Outline each Plasmodium vivax-infected red blood cell.
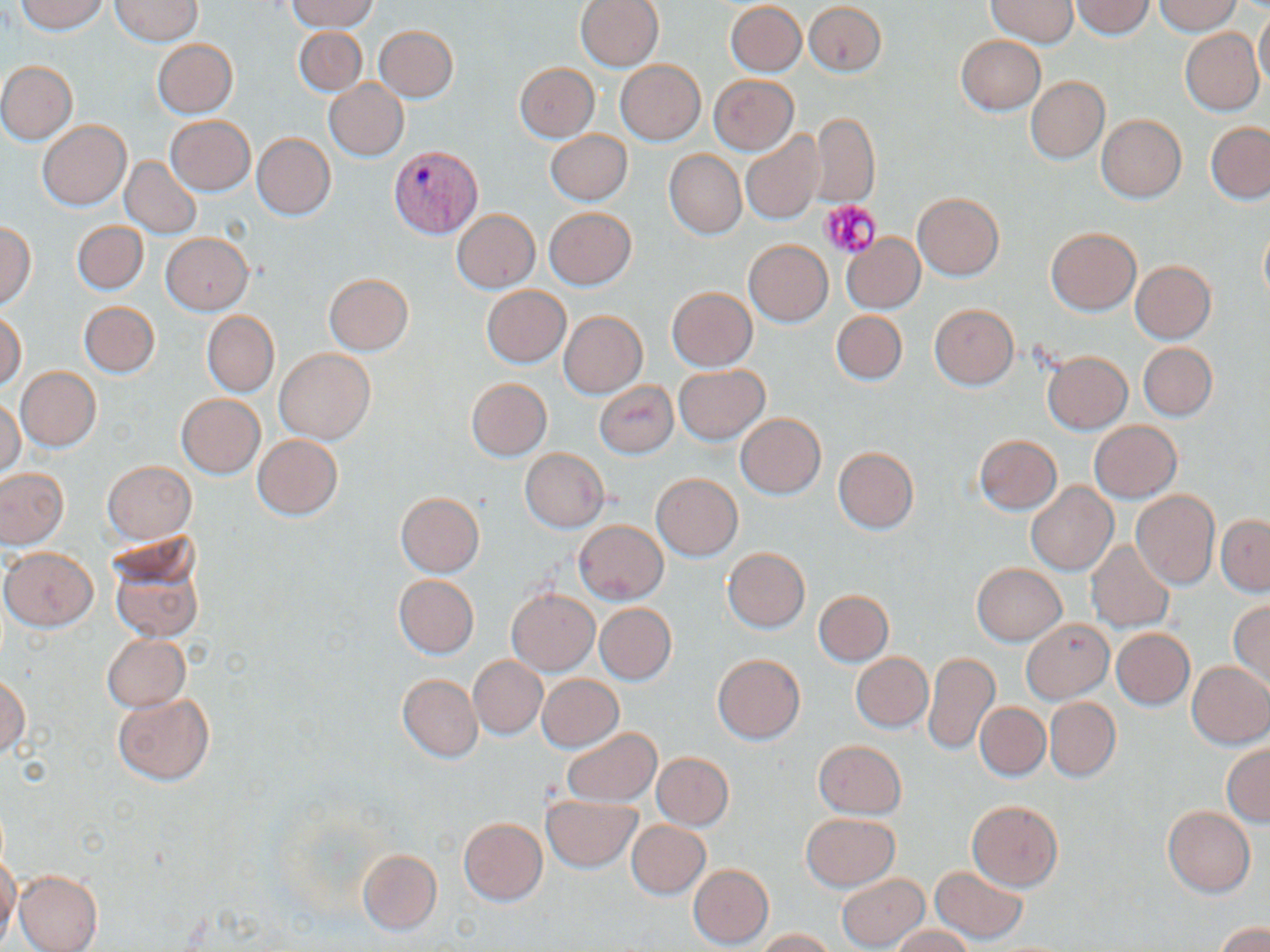
Approximate bounding boxes as named x1/y1/x2/y2 corners in pixels.
Plasmodium vivax-infected red blood cells: (x1=390, y1=151, x2=481, y2=240).

slide-level diagnosis = Plasmodium vivax
magnification = 1000x
platelet locations = approximate bounding boxes as named x1/y1/x2/y2 corners in pixels: (x1=821, y1=200, x2=883, y2=259)
stain = May-Grünwald-Giemsa
preparation = thin blood film
uninfected red blood cell locations = approximate bounding boxes as named x1/y1/x2/y2 corners in pixels: (x1=16, y1=0, x2=107, y2=35), (x1=109, y1=0, x2=202, y2=45), (x1=288, y1=0, x2=375, y2=33), (x1=575, y1=0, x2=664, y2=72), (x1=986, y1=0, x2=1078, y2=48), (x1=1070, y1=0, x2=1154, y2=39), (x1=1151, y1=0, x2=1242, y2=35), (x1=725, y1=2, x2=806, y2=76), (x1=803, y1=2, x2=887, y2=76), (x1=1254, y1=8, x2=1270, y2=90), (x1=374, y1=25, x2=458, y2=102), (x1=293, y1=26, x2=367, y2=96), (x1=1180, y1=28, x2=1264, y2=116), (x1=956, y1=35, x2=1046, y2=115), (x1=152, y1=39, x2=238, y2=119), (x1=615, y1=59, x2=706, y2=145), (x1=1, y1=61, x2=76, y2=144), (x1=514, y1=63, x2=599, y2=142), (x1=709, y1=74, x2=798, y2=155), (x1=1027, y1=77, x2=1109, y2=164), (x1=324, y1=80, x2=408, y2=161), (x1=812, y1=112, x2=879, y2=206), (x1=1097, y1=114, x2=1186, y2=202), (x1=166, y1=117, x2=254, y2=196), (x1=37, y1=120, x2=130, y2=211), (x1=1205, y1=122, x2=1270, y2=204), (x1=545, y1=130, x2=631, y2=205), (x1=740, y1=132, x2=825, y2=225), (x1=252, y1=134, x2=334, y2=220), (x1=664, y1=150, x2=746, y2=239), (x1=121, y1=157, x2=201, y2=238), (x1=912, y1=192, x2=1003, y2=280), (x1=544, y1=208, x2=637, y2=291), (x1=452, y1=209, x2=540, y2=293), (x1=72, y1=221, x2=146, y2=295), (x1=0, y1=223, x2=35, y2=307), (x1=1259, y1=225, x2=1270, y2=307), (x1=1046, y1=228, x2=1141, y2=315), (x1=161, y1=233, x2=253, y2=314), (x1=841, y1=234, x2=925, y2=313), (x1=743, y1=240, x2=833, y2=326), (x1=1131, y1=261, x2=1215, y2=343), (x1=324, y1=274, x2=414, y2=355), (x1=481, y1=286, x2=570, y2=369), (x1=666, y1=288, x2=756, y2=371), (x1=78, y1=301, x2=161, y2=378), (x1=929, y1=304, x2=1018, y2=389), (x1=559, y1=310, x2=647, y2=398), (x1=831, y1=310, x2=906, y2=386), (x1=0, y1=311, x2=25, y2=391), (x1=202, y1=311, x2=278, y2=397), (x1=1139, y1=342, x2=1217, y2=420), (x1=275, y1=349, x2=374, y2=444), (x1=1042, y1=350, x2=1132, y2=434), (x1=674, y1=365, x2=769, y2=445), (x1=16, y1=367, x2=100, y2=451), (x1=466, y1=378, x2=551, y2=461), (x1=594, y1=382, x2=678, y2=458), (x1=175, y1=395, x2=264, y2=480), (x1=0, y1=398, x2=24, y2=478), (x1=735, y1=414, x2=825, y2=498), (x1=1090, y1=421, x2=1181, y2=503), (x1=252, y1=435, x2=343, y2=519), (x1=975, y1=436, x2=1061, y2=514), (x1=833, y1=447, x2=918, y2=534), (x1=520, y1=449, x2=608, y2=532), (x1=102, y1=461, x2=195, y2=544), (x1=0, y1=469, x2=68, y2=549), (x1=651, y1=474, x2=742, y2=561), (x1=1026, y1=483, x2=1116, y2=575), (x1=1131, y1=490, x2=1220, y2=589), (x1=395, y1=492, x2=484, y2=577), (x1=1217, y1=515, x2=1270, y2=596), (x1=574, y1=520, x2=669, y2=603), (x1=1087, y1=541, x2=1174, y2=633), (x1=1, y1=548, x2=96, y2=631), (x1=109, y1=548, x2=203, y2=643), (x1=723, y1=548, x2=810, y2=632), (x1=972, y1=564, x2=1065, y2=645), (x1=392, y1=574, x2=477, y2=659), (x1=507, y1=590, x2=598, y2=674), (x1=813, y1=590, x2=893, y2=666), (x1=1229, y1=600, x2=1270, y2=689), (x1=594, y1=604, x2=676, y2=685), (x1=1022, y1=620, x2=1113, y2=703), (x1=1112, y1=628, x2=1194, y2=710), (x1=102, y1=635, x2=190, y2=712), (x1=924, y1=652, x2=1000, y2=755), (x1=852, y1=653, x2=932, y2=732), (x1=468, y1=655, x2=547, y2=739), (x1=712, y1=655, x2=805, y2=744), (x1=1187, y1=660, x2=1270, y2=748), (x1=397, y1=674, x2=482, y2=762), (x1=536, y1=674, x2=623, y2=752), (x1=0, y1=675, x2=29, y2=760), (x1=112, y1=692, x2=215, y2=787), (x1=1045, y1=697, x2=1120, y2=782), (x1=975, y1=702, x2=1049, y2=782), (x1=561, y1=727, x2=661, y2=808), (x1=814, y1=740, x2=905, y2=818), (x1=1223, y1=743, x2=1270, y2=826), (x1=652, y1=753, x2=734, y2=829), (x1=541, y1=794, x2=642, y2=872), (x1=966, y1=800, x2=1063, y2=891), (x1=1163, y1=806, x2=1255, y2=898), (x1=801, y1=814, x2=900, y2=890), (x1=458, y1=817, x2=547, y2=905), (x1=626, y1=820, x2=709, y2=899), (x1=357, y1=849, x2=441, y2=933), (x1=0, y1=853, x2=20, y2=945), (x1=688, y1=864, x2=773, y2=948), (x1=930, y1=866, x2=1028, y2=945), (x1=14, y1=871, x2=103, y2=952), (x1=836, y1=873, x2=929, y2=950), (x1=1216, y1=922, x2=1269, y2=952), (x1=893, y1=926, x2=975, y2=952), (x1=755, y1=928, x2=836, y2=952)
field of view = single
modality = optical microscopy
image size = 1270×952 pixels